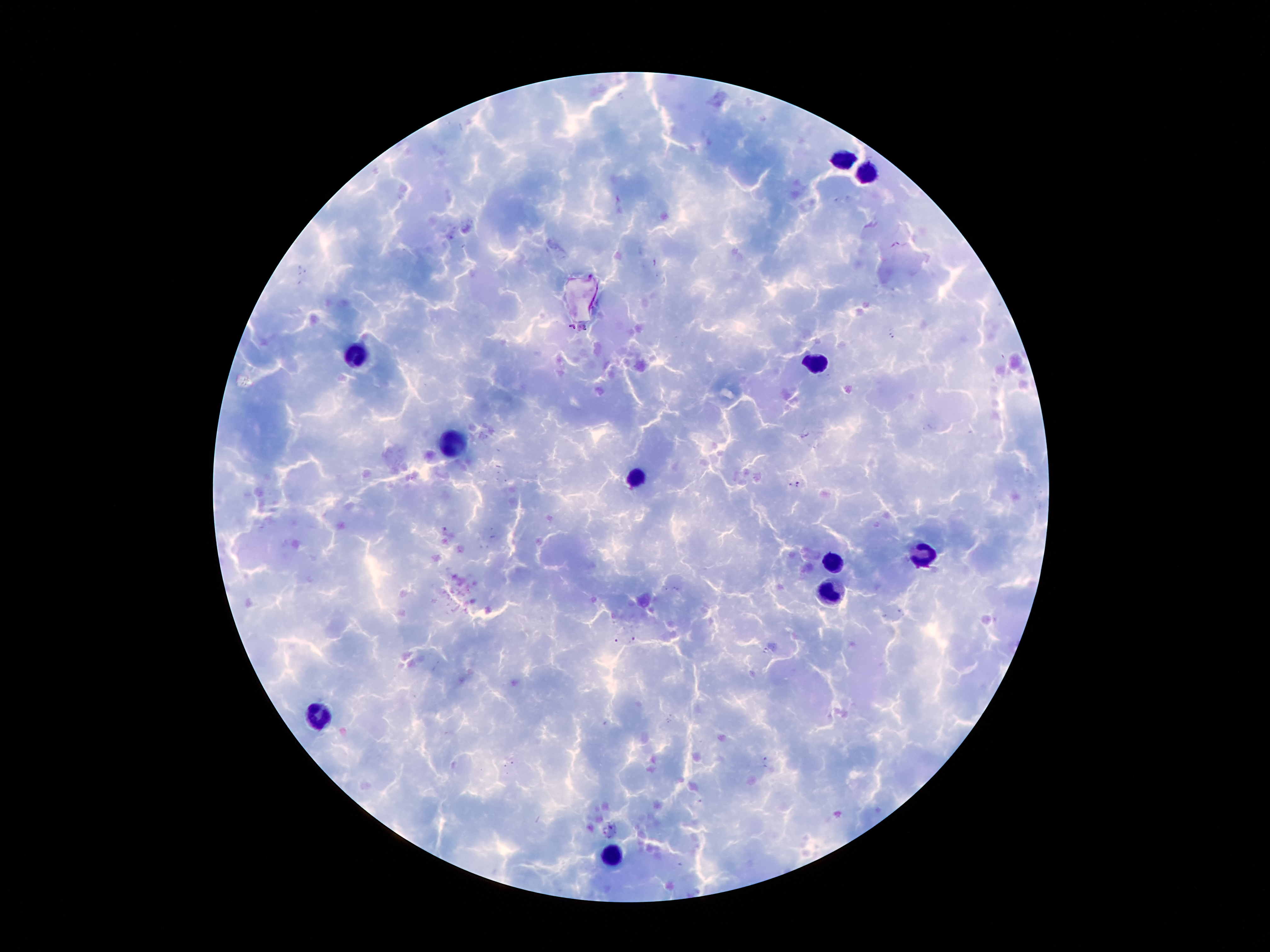
image_size: 1270×952 pixels
capture: smartphone through the microscope eyepiece
stain: Giemsa
field_of_view: one from this slide
malaria_parasites: not seen
preparation: thick blood smear
patient_malaria_status: infected with Plasmodium falciparum
leukocyte_locations: 'approximate centers as [x, y] in pixels: [844, 160], [868, 171], [359, 354], [818, 364], [451, 443], [639, 476], [917, 558], [836, 561], [828, 589], [316, 714], [615, 856]'
magnification: 100x